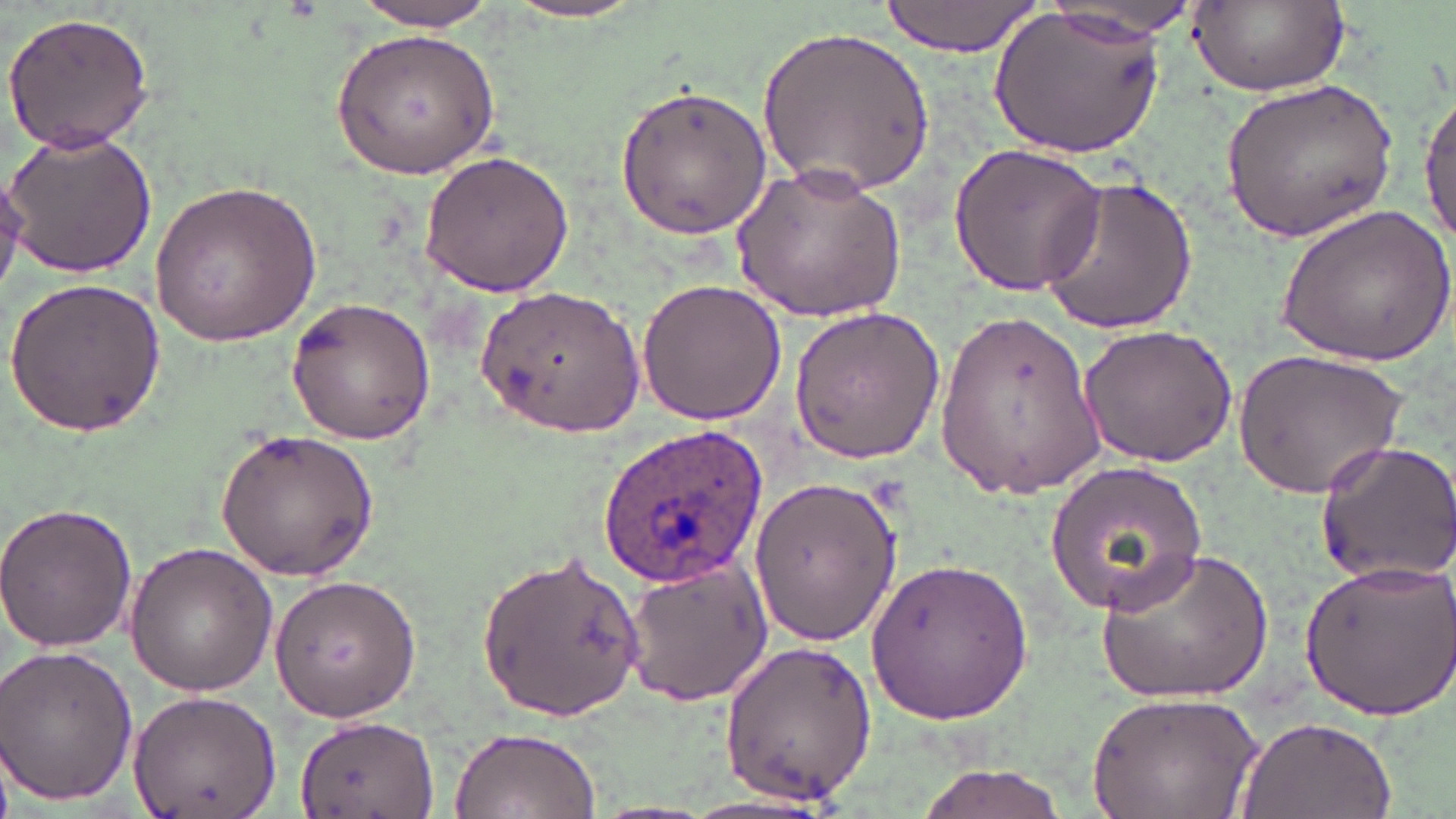
Approximate bounding boxes as [x1, y1, x2, y2] in pixels. Plasmodium ovale-infected red blood cell locations: [595, 422, 769, 588]. Uninfected red blood cell locations: [1042, 0, 1211, 40], [1188, 0, 1346, 99], [346, 1, 508, 33], [503, 1, 650, 24], [878, 1, 1044, 57], [990, 4, 1165, 160], [3, 11, 157, 153], [757, 24, 933, 196], [331, 28, 499, 179], [1220, 74, 1397, 242], [1419, 82, 1456, 254], [615, 83, 773, 240], [1, 129, 157, 277], [946, 139, 1110, 299], [418, 150, 577, 297], [730, 161, 906, 325], [1036, 174, 1198, 337], [150, 178, 321, 345], [1274, 205, 1453, 367], [4, 278, 164, 437], [635, 278, 786, 424], [477, 285, 645, 435], [286, 296, 437, 445], [787, 304, 951, 464], [935, 312, 1105, 495], [1077, 324, 1241, 469], [1235, 346, 1408, 500], [212, 430, 379, 582], [1314, 440, 1456, 585], [1044, 459, 1210, 617], [748, 474, 902, 648], [0, 501, 138, 654], [122, 542, 278, 698], [476, 544, 646, 721], [1096, 546, 1273, 702], [622, 554, 772, 705], [867, 554, 1033, 726], [1296, 556, 1455, 721], [269, 572, 422, 722], [714, 639, 877, 805], [0, 643, 138, 807], [1089, 689, 1260, 819], [126, 692, 281, 814], [1234, 712, 1398, 819], [294, 716, 440, 817], [445, 726, 601, 819], [912, 763, 1078, 818]. Slide-level diagnosis: Plasmodium ovale. Light microscopy. Image is 1456×819 pixels. One field of a larger specimen. Captured at 1000x magnification. May-Grünwald-Giemsa stain. Thin blood film.